Identify the parasite.
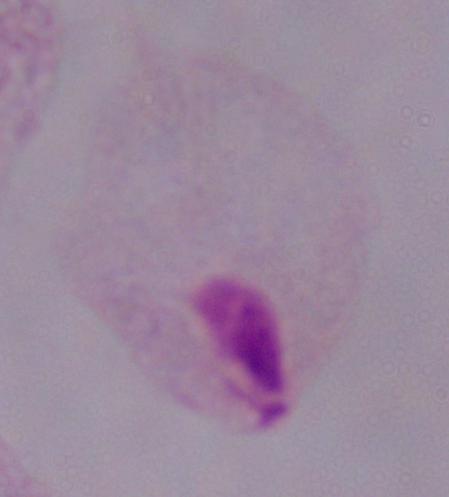
This is a trichomonad.

magnification = 1000x
modality = micrograph